Comment on the morphology of the red blood cells.
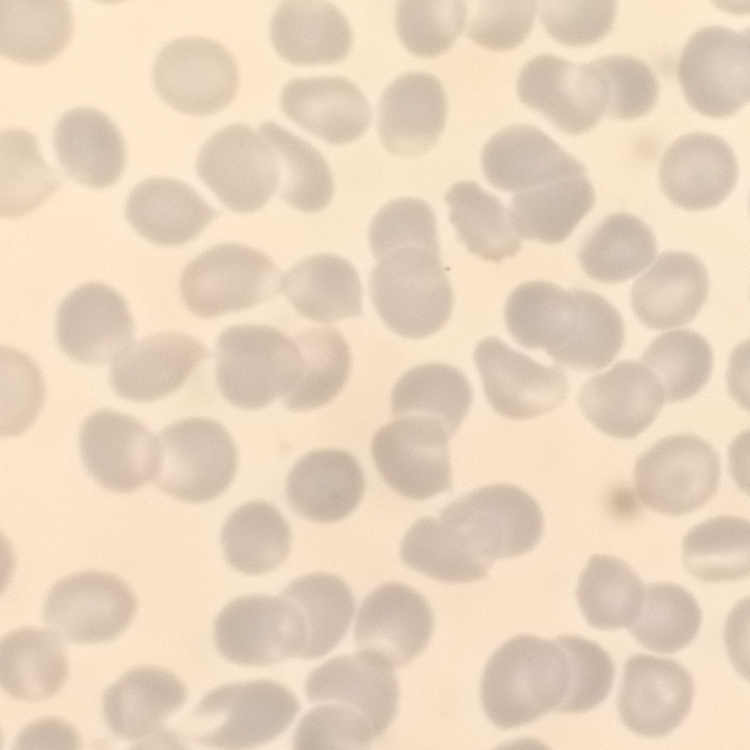
They show no rouleaux formation.

Summary:
  - Preparation: thin peripheral smear
  - Image type: one tile cut from a larger photomicrograph
  - Stain: Field's or Giemsa